Locate malaria parasites and leukocytes.
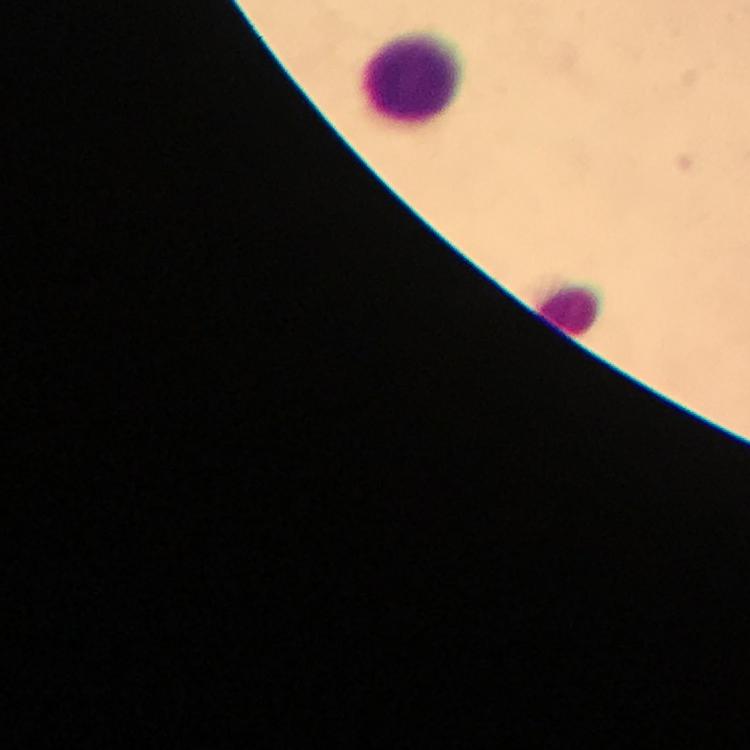

No malaria parasites seen.
Approximate centers as [x, y] in pixels.
Leukocytes: [412, 77], [571, 308].

cropped_from: one field of view
magnification: 100x
stain: Giemsa
immersion_oil: applied
capture: smartphone camera through the microscope
context: from a malaria diagnostic workup
preparation: thick blood film
image_size: 750×750 pixels